Classify this cell by malaria status.
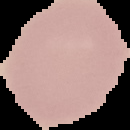
It is uninfected.

Image is 130×130 pixels. From a thin blood smear. Segmented cell region on a black background.